Locate every leukocyte (white blood cell).
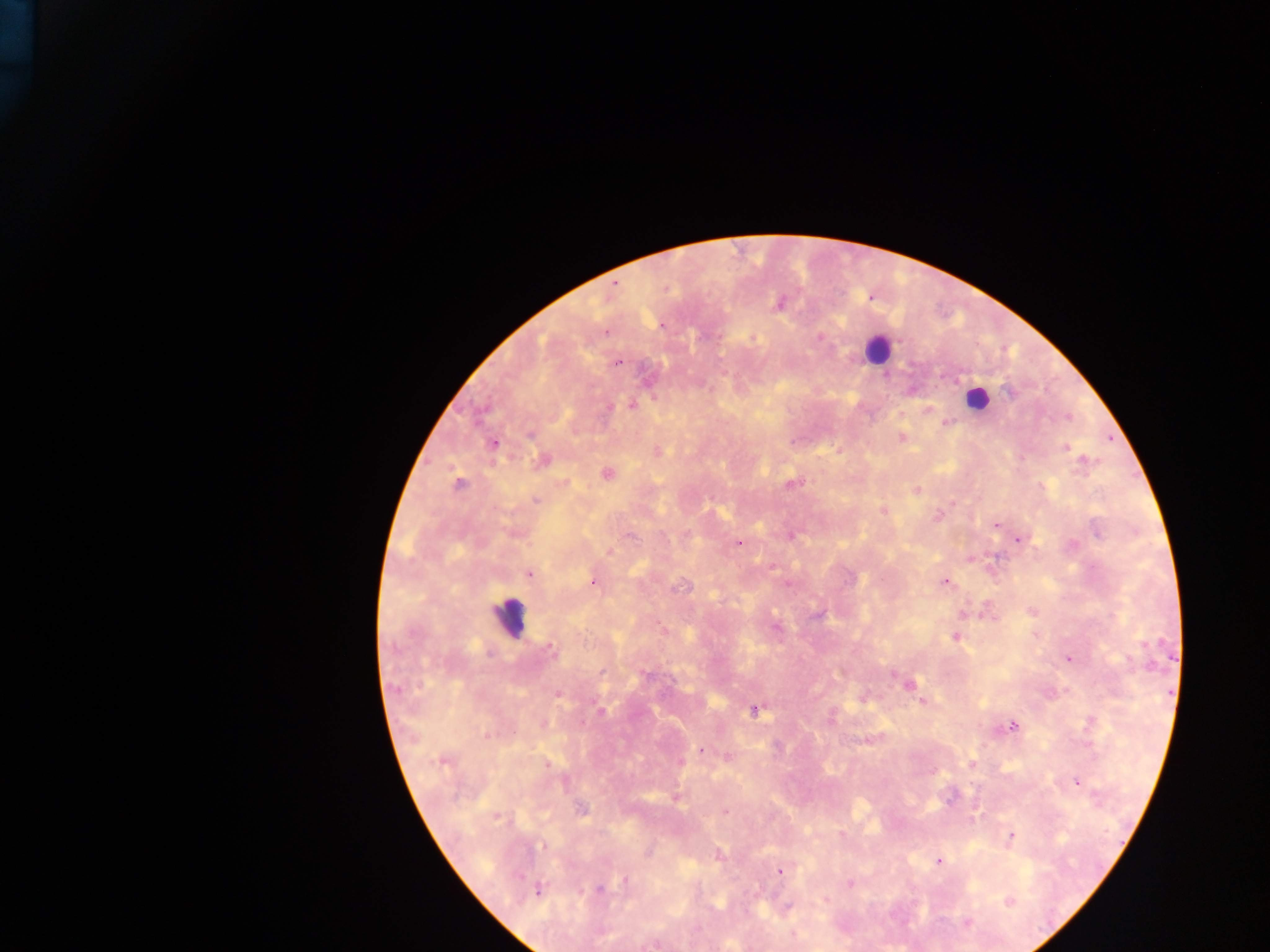
Approximate centers as x y in pixels.
Leukocytes: 877 347; 508 617.

Summary:
  - Plasmodium parasite locations: 782 301; 778 304; 819 335; 753 339; 616 362; 1009 391; 654 398; 974 398; 984 399; 631 403; 606 406; 928 409; 1067 417; 944 424; 901 438; 1066 448; 656 451; 1082 461; 540 462; 607 473; 459 482; 788 483; 916 488; 536 499; 882 509; 942 510; 938 515; 994 525; 686 533; 629 536; 1019 540; 739 544; 609 551; 529 574; 592 581; 945 582; 679 587; 964 612; 1029 612; 777 628; 662 629; 956 638; 550 649; 1069 658; 840 672; 910 684; 396 687; 558 694; 863 699; 923 702; 755 711; 832 715; 1011 725; 487 735; 702 750; 725 756; 972 762; 547 763; 933 773; 1076 782; 949 799; 975 812; 725 813; 841 833; 1010 837; 542 845; 649 851; 940 861; 781 870; 623 880; 848 883; 599 889; 825 899; 1009 900; 969 923; 652 944
  - Country: Ghana
  - Image size: 1270×952 pixels
  - Field of view: single
  - Capture: mobile-phone photograph through a microscope
  - Preparation: thick blood film